Outline each uninfected red blood cell.
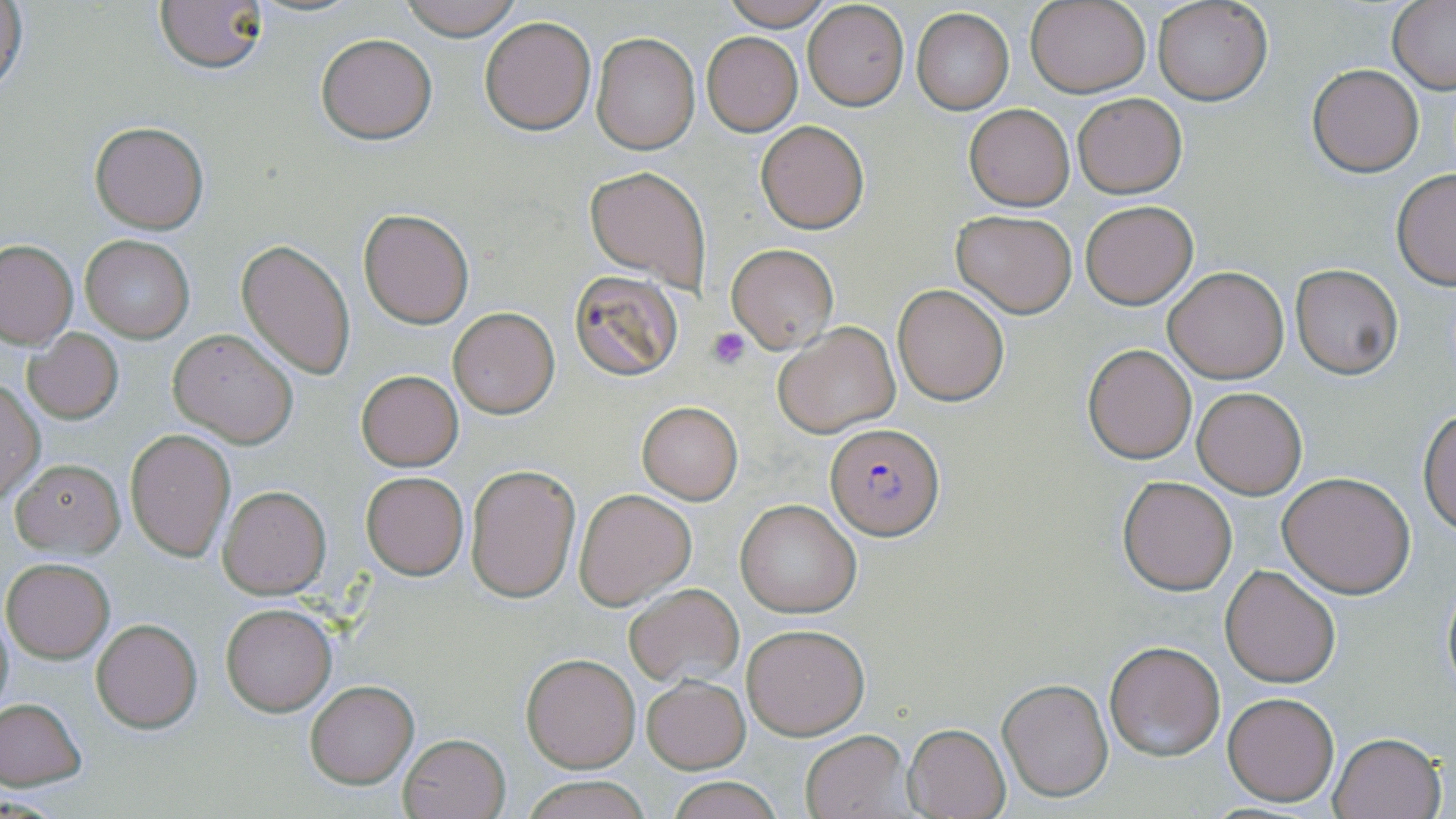

Approximate bounding boxes as (x1, y1, x2, y2) in pixels.
Uninfected red blood cells: (1, 0, 27, 101), (155, 0, 269, 73), (396, 0, 524, 40), (717, 0, 838, 29), (1026, 0, 1150, 97), (1152, 0, 1271, 105), (1388, 1, 1456, 92), (803, 2, 909, 110), (911, 9, 1013, 114), (479, 17, 596, 134), (315, 32, 437, 144), (592, 32, 699, 154), (701, 32, 802, 135), (1308, 64, 1423, 176), (1072, 93, 1188, 199), (964, 104, 1074, 211), (89, 120, 208, 233), (756, 120, 869, 233), (584, 165, 711, 288), (1392, 167, 1456, 289), (1080, 200, 1197, 309), (359, 208, 473, 328), (950, 209, 1077, 316), (79, 234, 195, 342), (238, 239, 356, 378), (0, 240, 77, 347), (726, 244, 838, 352), (1290, 264, 1402, 379), (1162, 266, 1289, 383), (568, 269, 684, 382), (893, 283, 1011, 405), (448, 308, 559, 418), (773, 321, 900, 439), (169, 329, 298, 447), (24, 330, 123, 423), (1083, 344, 1195, 464), (356, 369, 464, 471), (0, 378, 45, 506), (1193, 387, 1306, 498), (637, 401, 743, 505), (1419, 405, 1456, 535), (125, 429, 236, 561), (11, 458, 125, 558), (465, 464, 581, 602), (361, 471, 468, 580), (1277, 472, 1415, 598), (1117, 476, 1237, 593), (218, 485, 330, 598), (573, 488, 696, 610), (736, 498, 860, 618), (2, 558, 114, 663), (1220, 565, 1342, 686), (1441, 576, 1456, 697), (622, 584, 744, 688), (221, 603, 336, 716), (92, 619, 203, 733), (742, 624, 869, 739), (1104, 640, 1225, 760), (520, 652, 640, 773), (642, 675, 749, 773), (997, 678, 1114, 804), (304, 680, 418, 787), (1222, 690, 1340, 807), (0, 698, 87, 789), (903, 723, 1011, 818), (800, 729, 909, 817), (398, 732, 509, 819), (1330, 732, 1446, 819), (522, 774, 653, 819), (665, 774, 783, 819).

Summary:
  - Platelet locations: (705, 326, 752, 368)
  - Plasmodium falciparum-infected red blood cell locations: (827, 423, 943, 538)
  - Slide-level diagnosis: Plasmodium falciparum
  - Stain: May-Grünwald-Giemsa
  - Modality: light microscopy
  - Image size: 1456×819 pixels
  - Preparation: thin blood smear
  - Field of view: one of a larger specimen
  - Magnification: 1000x